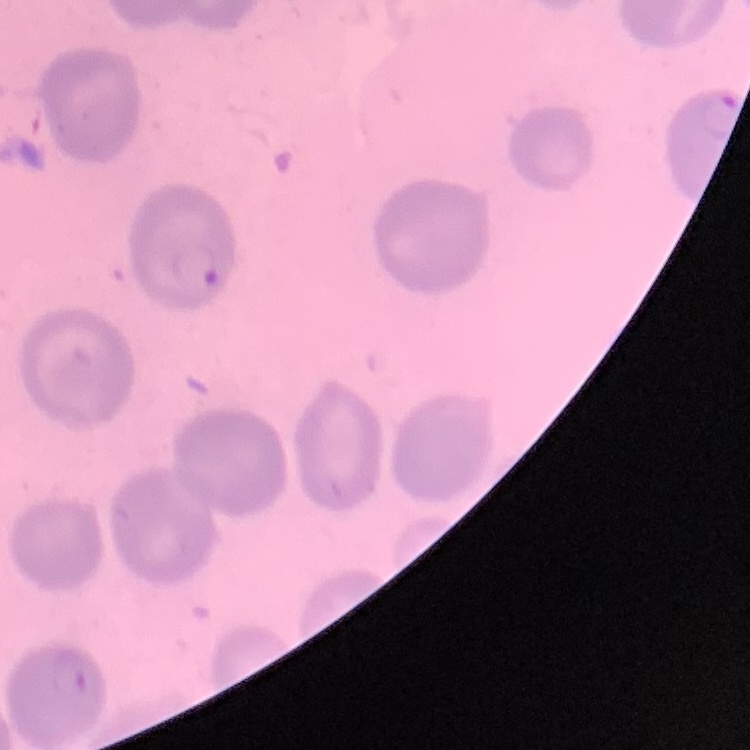

erythrocyte_morphology: no rouleaux formation
image_type: one tile cut from a larger photomicrograph
stain: Field's or Giemsa
preparation: thin blood smear